Report the malaria status of this cell.
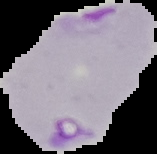

Parasitized.

Summary:
  - Image size: 157×154 pixels
  - Image type: cell region segmented out of the field of view; surrounding area masked to black
  - Preparation: thin blood smear